State the preparation type.
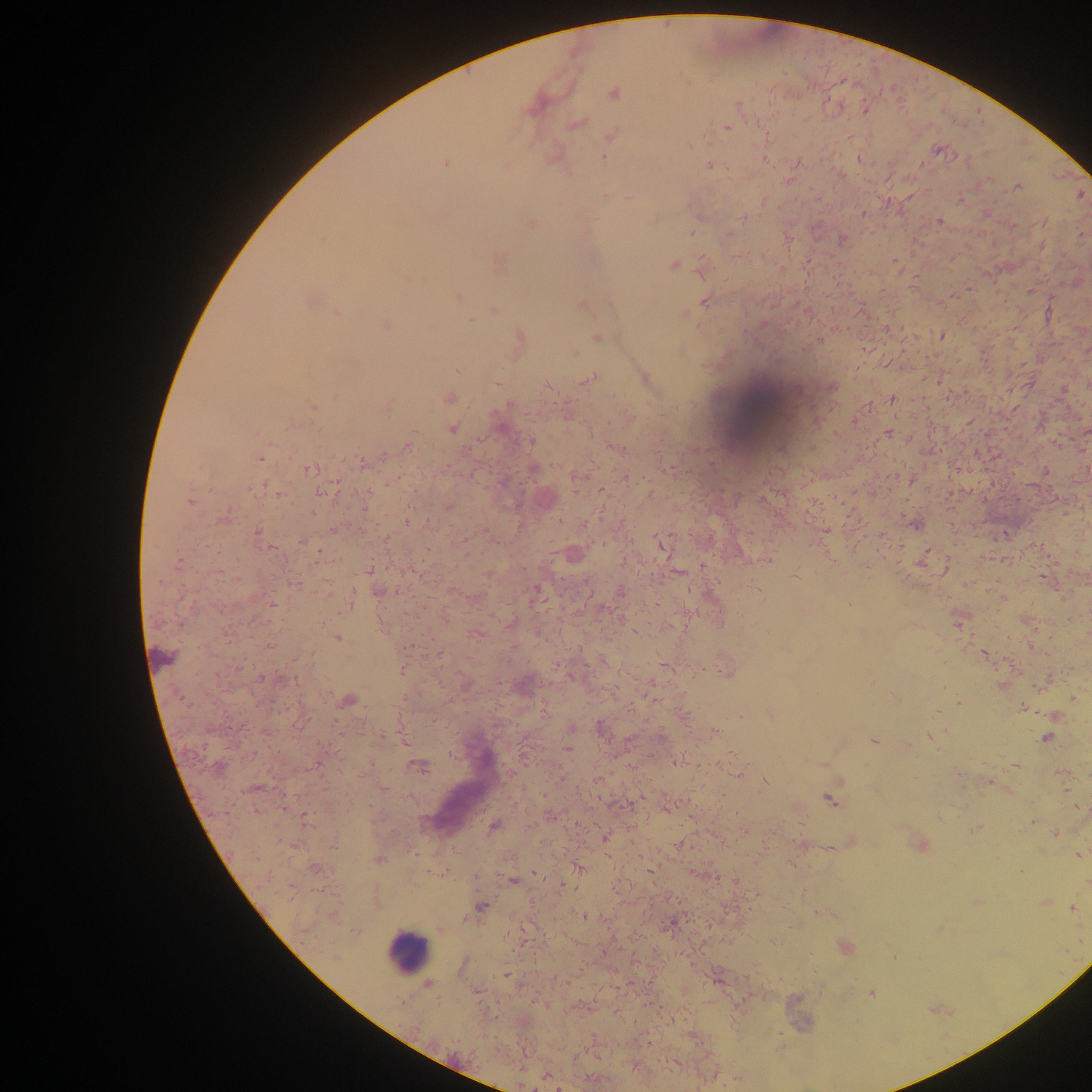
This is a thick smear.

Approximate centers as [x, y] in pixels. Leukocyte locations: [756, 410], [407, 951]. Malaria parasite locations: [613, 93], [578, 123], [727, 129], [612, 136], [689, 145], [937, 149], [604, 158], [445, 163], [507, 164], [710, 165], [1017, 186], [606, 197], [630, 198], [863, 213], [742, 218], [939, 221], [530, 224], [692, 232], [729, 234], [841, 239], [499, 261], [672, 265], [702, 270], [458, 297], [309, 301], [705, 301], [580, 305], [494, 310], [337, 314], [685, 314], [470, 320], [386, 325], [942, 336], [597, 337], [818, 341], [457, 370], [645, 377], [589, 379], [497, 383], [832, 387], [335, 396], [450, 397], [891, 399], [388, 406], [313, 407], [629, 418], [289, 425], [501, 427], [452, 429], [1086, 431], [889, 433], [531, 442], [408, 444], [614, 447], [261, 457], [364, 463], [309, 470], [1045, 471], [624, 476], [911, 481], [265, 485], [189, 502], [225, 516], [408, 519], [914, 524], [256, 532], [1005, 534], [661, 543], [270, 547], [319, 552], [573, 554], [767, 560], [703, 567], [487, 574], [796, 576], [295, 584], [379, 591], [536, 591], [621, 593], [272, 606], [345, 610], [720, 624], [337, 637], [269, 646], [440, 655], [984, 655], [724, 670], [401, 671], [261, 679], [1002, 685], [466, 686], [896, 698], [1073, 698], [348, 700], [959, 703], [1023, 708], [770, 714], [1053, 715], [741, 716], [599, 727], [715, 732], [932, 737], [1046, 738], [873, 741], [404, 742], [567, 750], [678, 761], [822, 764], [315, 765], [1016, 765], [419, 768], [739, 773], [765, 781], [987, 783], [253, 788], [383, 789], [830, 801], [305, 816], [940, 818], [1033, 821], [494, 827], [975, 830], [1055, 834], [605, 837], [679, 845], [1080, 855], [378, 859], [315, 868], [579, 869], [536, 873], [512, 881], [734, 882], [290, 891], [1045, 902], [481, 907], [1071, 909], [583, 915], [671, 924], [895, 956], [505, 975], [719, 979], [428, 984], [872, 994]. Collected in Ghana. Image is 1092×1092 pixels. One field of view. Mobile-phone photograph taken through the microscope.